Give the position of every Plasmodium parasite visible.
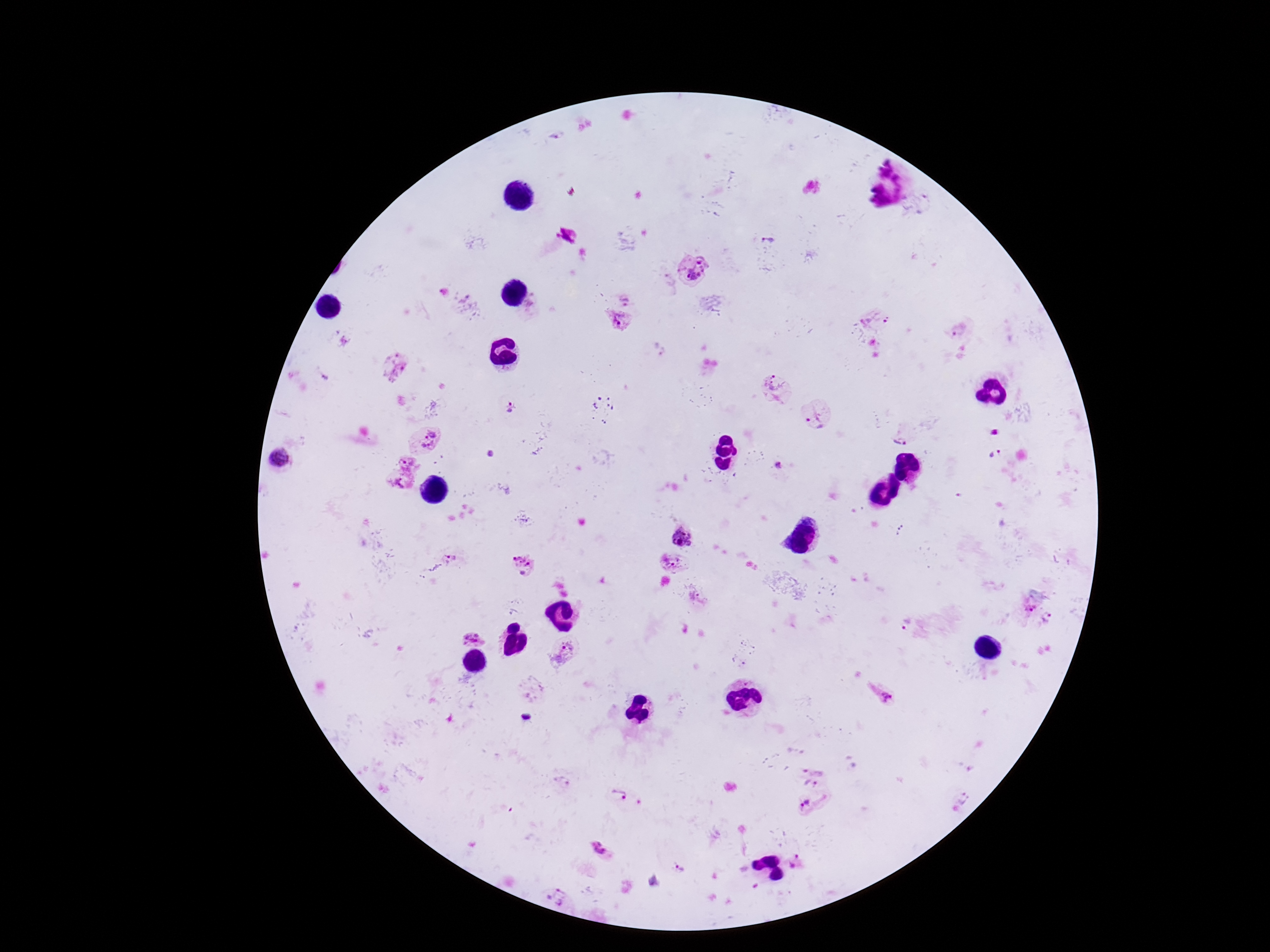
Approximate centers as {x, y} in pixels.
Plasmodium parasites: {769, 237}, {695, 270}, {624, 299}, {878, 316}, {617, 320}, {960, 329}, {394, 365}, {775, 388}, {597, 401}, {509, 407}, {816, 415}, {904, 431}, {422, 439}, {995, 455}, {283, 460}, {780, 467}, {402, 473}, {681, 536}, {451, 556}, {523, 563}, {675, 564}, {1030, 606}, {1048, 617}, {906, 623}, {473, 636}, {563, 651}, {881, 693}, {526, 717}, {813, 772}, {564, 782}, {618, 793}, {815, 805}, {600, 848}, {795, 863}, {680, 867}, {558, 896}.

Summary:
  - Field of view: one from this slide
  - Magnification: 100x
  - Patient malaria status: positive
  - Preparation: thick peripheral-blood smear
  - Image size: 1270×952 pixels
  - Capture: smartphone camera through the microscope eyepiece
  - Stain: Giemsa